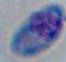

Summary:
  - Identification: Toxoplasma gondii
  - Magnification: 1000x
  - Modality: micrograph